Report the malaria status of this cell.
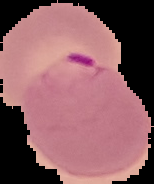

Parasitized.

preparation = thin blood film
image size = 154×184 pixels
image type = segmented cell region with the area outside set to black